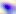
magnification = 400x
modality = photomicrograph
identification = Toxoplasma gondii